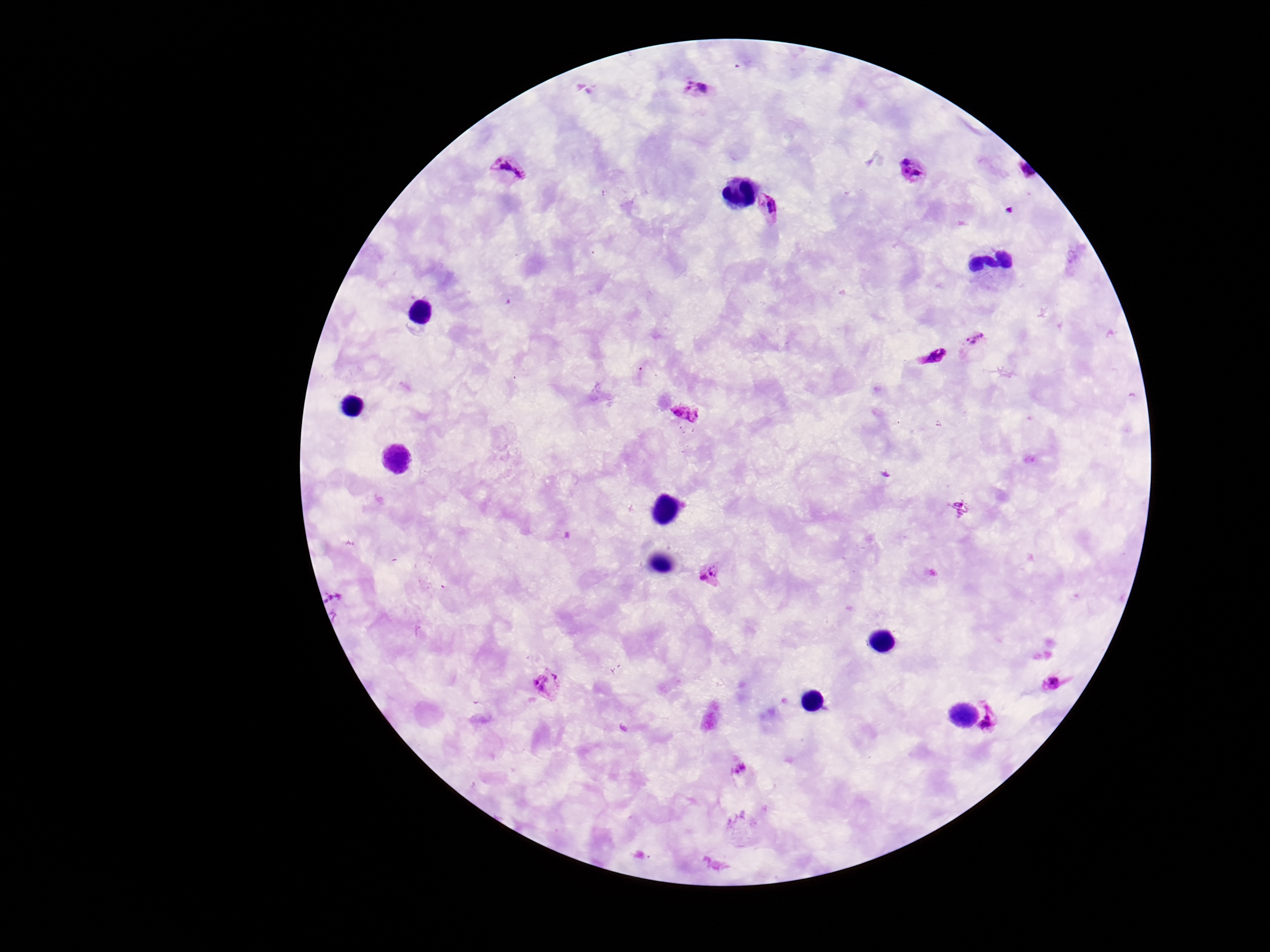
image size = 1270×952 pixels
capture = smartphone camera through the microscope eyepiece
Plasmodium parasite locations = approximate centers as [x, y] in pixels: [698, 91], [510, 171], [913, 172], [770, 206], [975, 344], [933, 357], [686, 413], [709, 574], [546, 685], [1057, 686], [992, 721], [742, 773]
field of view = single
stain = Giemsa
preparation = thick blood film
magnification = 100x
patient malaria status = positive